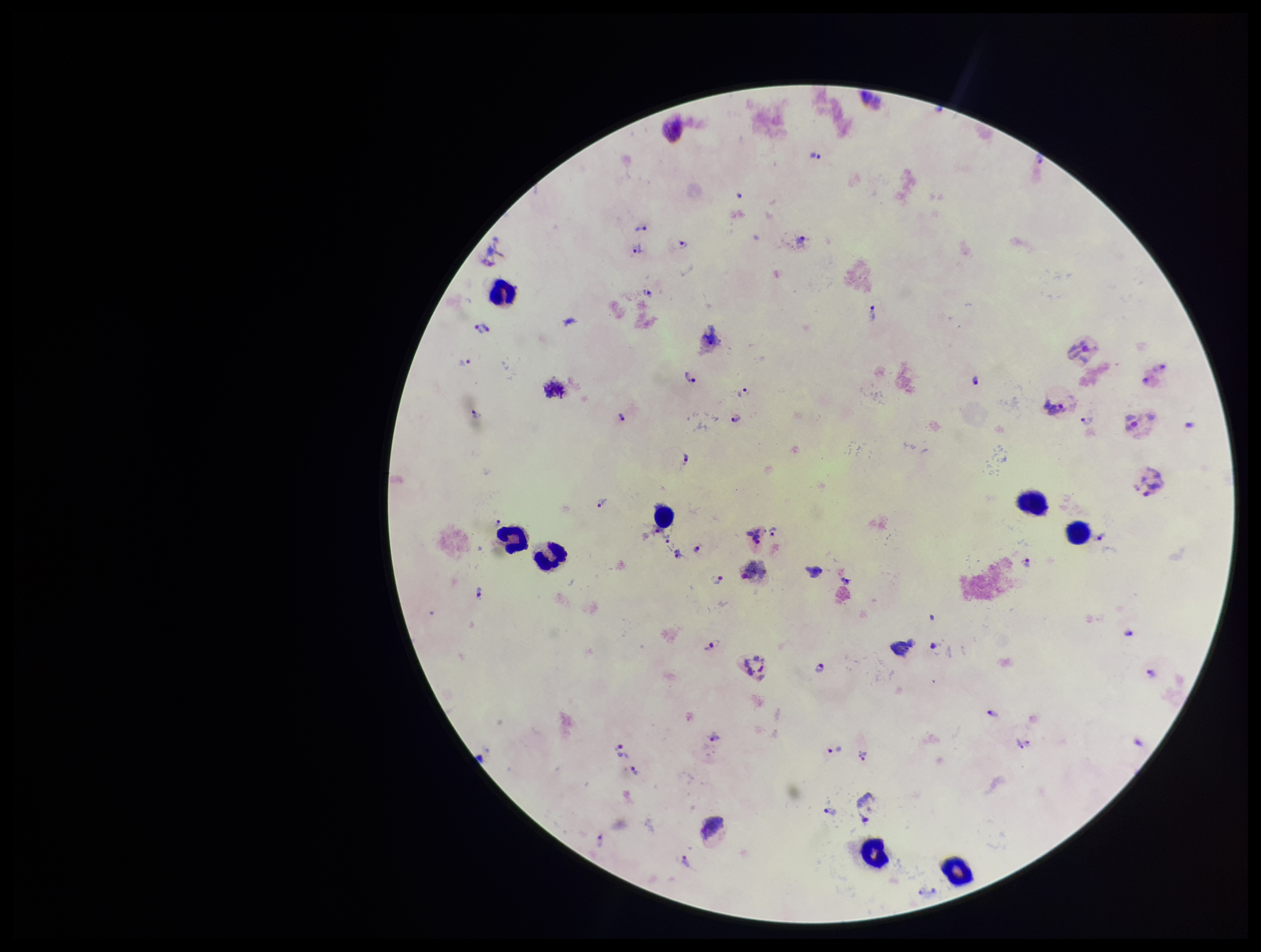
{
  "image_size": "1261×952 pixels",
  "leukocyte_count": 8,
  "plasmodium_parasites": "identified",
  "species_reported_for_this_patient": "Plasmodium vivax",
  "parasite_count": 43,
  "stain": "Giemsa",
  "field_of_view": "one from this slide",
  "capture": "smartphone photograph through the microscope eyepiece",
  "patient_malaria_status": "positive",
  "preparation": "thick blood smear"
}